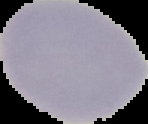

From a thin blood smear. Result: no Plasmodium parasites seen. Image is 148×124 pixels. Cell region segmented out of the field of view; the surrounding area is masked to black.